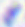

{
  "modality": "micrograph",
  "magnification": "400x",
  "identification": "Toxoplasma gondii"
}